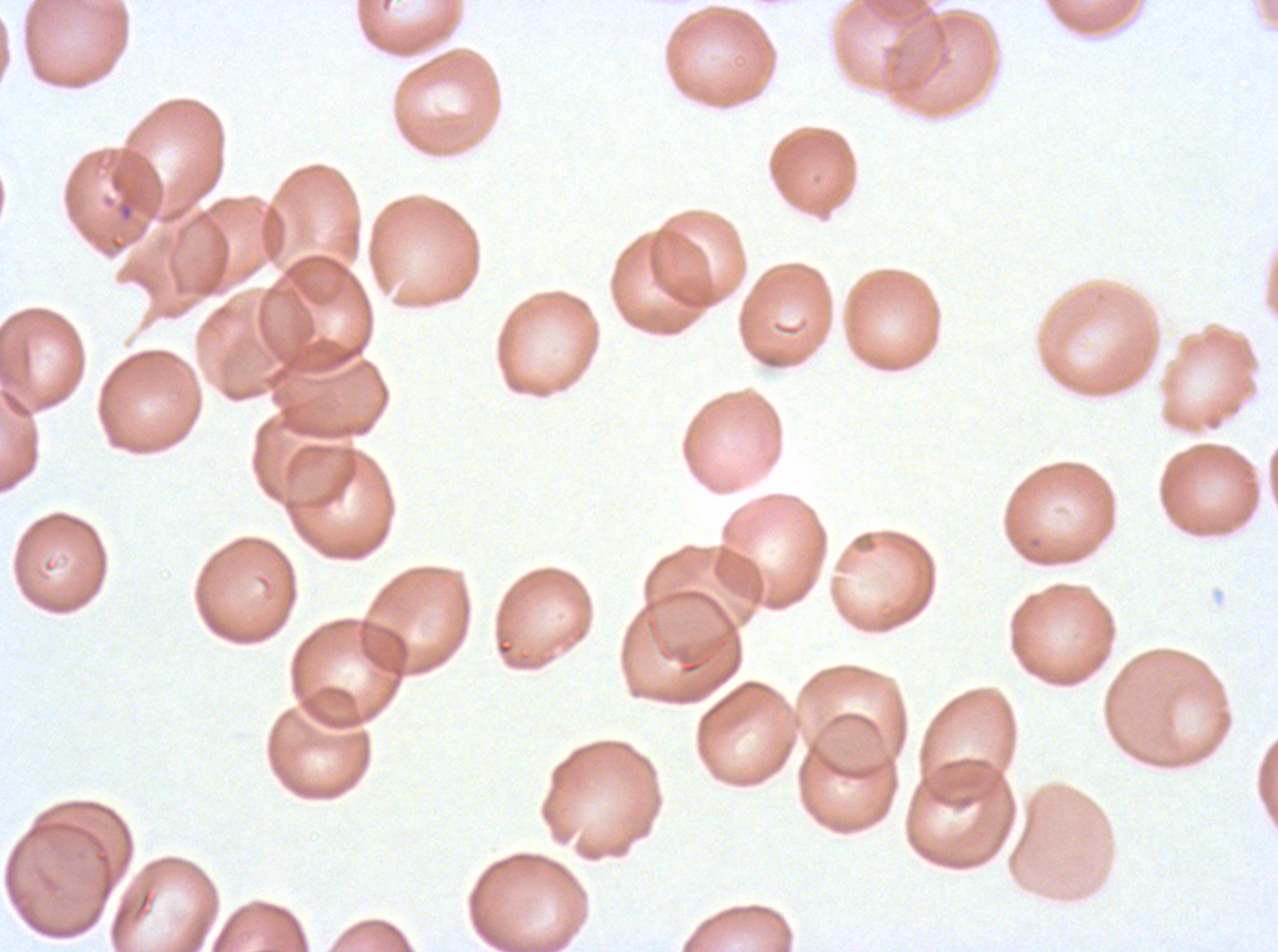 Approximate bounding boxes as [x1, y1, x2, y2] in pixels. Debris locations: [117, 201, 134, 222]. Giemsa stain. Thin blood smear. Ex-vivo Plasmodium falciparum culture from a patient in The Gambia, grown for 24 to 48 hours. One sub-image of a larger composite. Image is 1278×952 pixels.